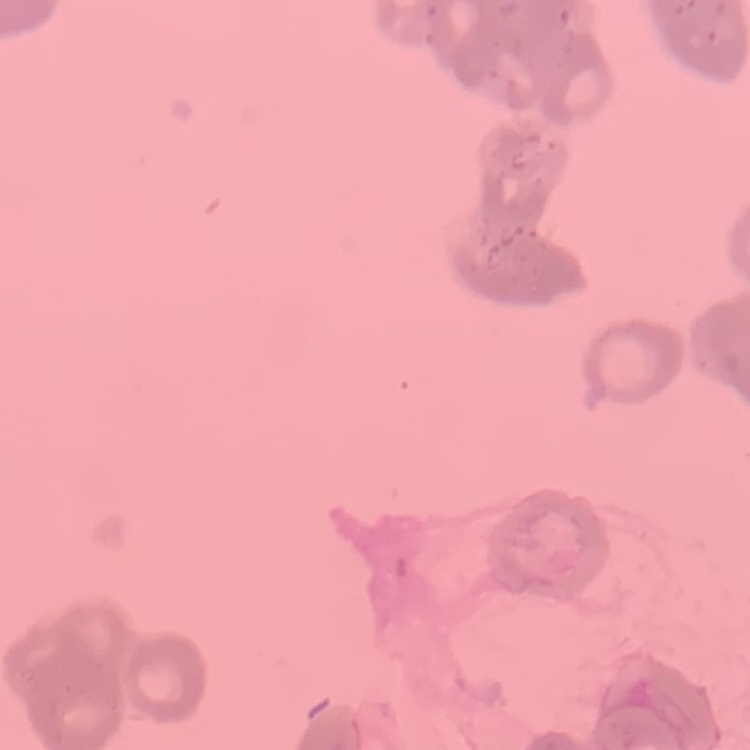 The erythrocytes show rouleaux formation. Square crop of a larger photomicrograph. Field's or Giemsa stain. Thin blood film.